Locate every blood parasite and identify its species.
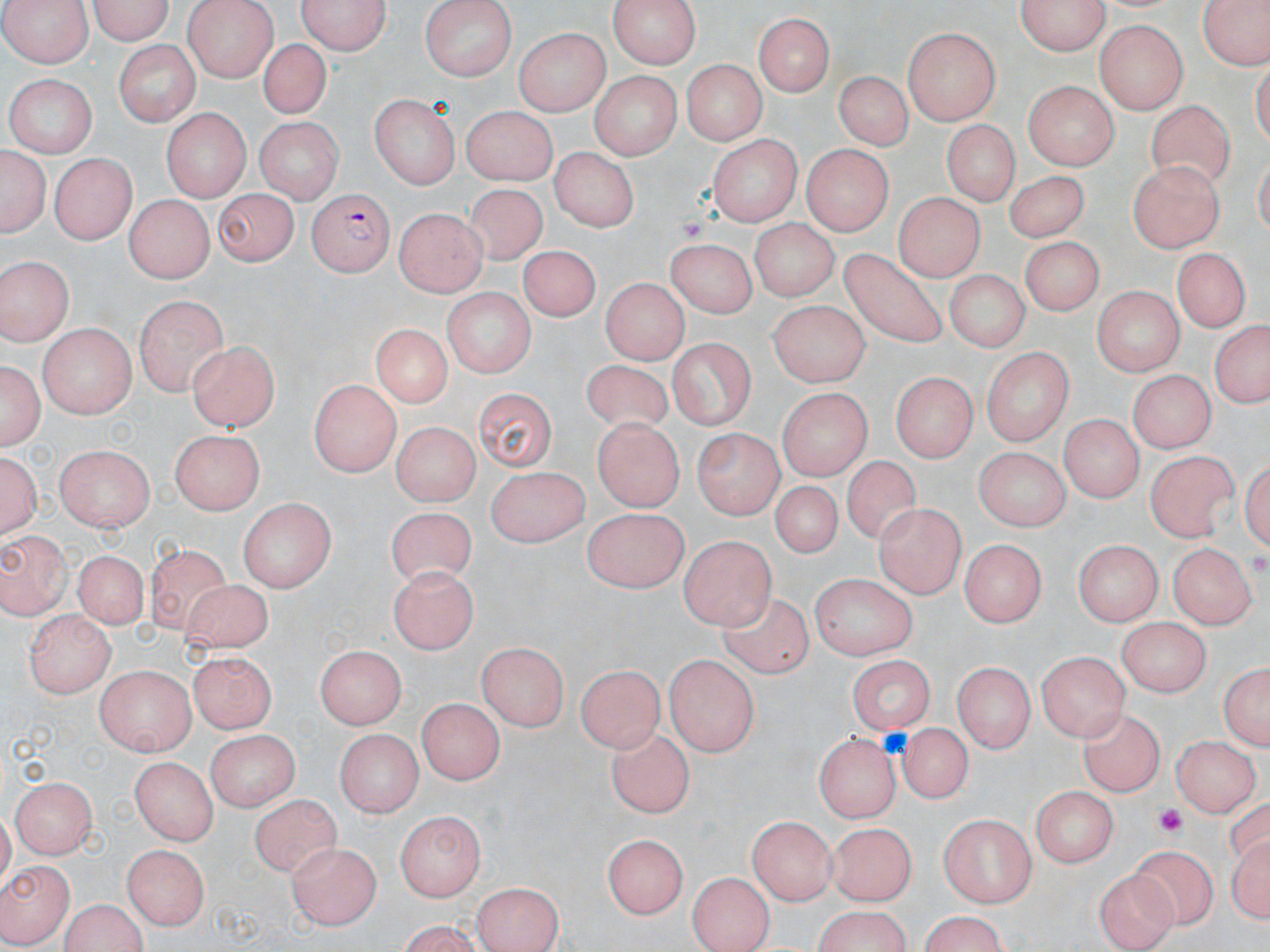

Approximate bounding boxes as named x1/y1/x2/y2 corners in pixels.
Plasmodium falciparum-infected red blood cells: (x1=305, y1=191, x2=393, y2=277).
No Plasmodium ovale, Plasmodium malariae, Plasmodium vivax, Babesia divergens, or Trypanosoma brucei observed.

slide-level diagnosis = Plasmodium falciparum
platelet locations = approximate bounding boxes as named x1/y1/x2/y2 corners in pixels: (x1=678, y1=215, x2=711, y2=245), (x1=1153, y1=802, x2=1192, y2=838)
modality = light microscopy
magnification = 1000x
uninfected red blood cell locations = approximate bounding boxes as named x1/y1/x2/y2 corners in pixels: (x1=83, y1=0, x2=179, y2=43), (x1=182, y1=0, x2=275, y2=79), (x1=296, y1=0, x2=392, y2=56), (x1=419, y1=0, x2=517, y2=78), (x1=606, y1=0, x2=705, y2=69), (x1=1016, y1=0, x2=1111, y2=55), (x1=1199, y1=0, x2=1267, y2=74), (x1=2, y1=1, x2=93, y2=68), (x1=1034, y1=9, x2=1162, y2=81), (x1=754, y1=10, x2=837, y2=97), (x1=1096, y1=20, x2=1188, y2=112), (x1=515, y1=26, x2=607, y2=112), (x1=904, y1=27, x2=1004, y2=124), (x1=256, y1=38, x2=334, y2=118), (x1=113, y1=40, x2=200, y2=126), (x1=679, y1=58, x2=765, y2=145), (x1=586, y1=70, x2=681, y2=160), (x1=836, y1=70, x2=908, y2=151), (x1=4, y1=74, x2=98, y2=155), (x1=1021, y1=79, x2=1120, y2=167), (x1=367, y1=95, x2=461, y2=189), (x1=1147, y1=97, x2=1235, y2=196), (x1=458, y1=105, x2=558, y2=183), (x1=163, y1=111, x2=248, y2=201), (x1=255, y1=119, x2=340, y2=202), (x1=943, y1=121, x2=1023, y2=208), (x1=706, y1=131, x2=802, y2=224), (x1=800, y1=144, x2=896, y2=233), (x1=2, y1=146, x2=49, y2=237), (x1=548, y1=148, x2=639, y2=231), (x1=48, y1=154, x2=137, y2=245), (x1=1127, y1=161, x2=1224, y2=254), (x1=1006, y1=167, x2=1088, y2=242), (x1=460, y1=182, x2=559, y2=270), (x1=210, y1=191, x2=297, y2=266), (x1=895, y1=192, x2=980, y2=281), (x1=121, y1=197, x2=212, y2=285), (x1=395, y1=205, x2=486, y2=295), (x1=747, y1=220, x2=837, y2=306), (x1=1025, y1=235, x2=1104, y2=313), (x1=671, y1=238, x2=755, y2=315), (x1=516, y1=247, x2=606, y2=330), (x1=1173, y1=247, x2=1252, y2=330), (x1=840, y1=248, x2=951, y2=353), (x1=0, y1=255, x2=72, y2=345), (x1=947, y1=267, x2=1029, y2=356), (x1=602, y1=278, x2=686, y2=367), (x1=1094, y1=285, x2=1182, y2=380), (x1=442, y1=287, x2=537, y2=378), (x1=135, y1=294, x2=228, y2=394), (x1=769, y1=298, x2=872, y2=385), (x1=37, y1=321, x2=136, y2=416), (x1=1206, y1=322, x2=1270, y2=411), (x1=365, y1=323, x2=459, y2=407), (x1=669, y1=340, x2=755, y2=428), (x1=187, y1=341, x2=278, y2=433), (x1=980, y1=347, x2=1073, y2=445), (x1=1, y1=356, x2=45, y2=454), (x1=581, y1=359, x2=677, y2=438), (x1=1128, y1=369, x2=1211, y2=452), (x1=893, y1=373, x2=975, y2=463), (x1=307, y1=383, x2=402, y2=474), (x1=474, y1=386, x2=558, y2=470), (x1=781, y1=387, x2=874, y2=477), (x1=1061, y1=413, x2=1141, y2=506), (x1=592, y1=419, x2=683, y2=511), (x1=389, y1=421, x2=480, y2=507), (x1=169, y1=426, x2=267, y2=513), (x1=694, y1=428, x2=782, y2=520), (x1=57, y1=445, x2=154, y2=532), (x1=978, y1=447, x2=1067, y2=534), (x1=1, y1=450, x2=42, y2=542), (x1=1149, y1=451, x2=1242, y2=542), (x1=840, y1=456, x2=927, y2=548), (x1=483, y1=466, x2=590, y2=548), (x1=768, y1=480, x2=845, y2=558), (x1=235, y1=500, x2=337, y2=593), (x1=874, y1=501, x2=964, y2=598), (x1=382, y1=506, x2=475, y2=595), (x1=584, y1=509, x2=686, y2=595), (x1=0, y1=528, x2=74, y2=617), (x1=680, y1=533, x2=773, y2=628), (x1=955, y1=537, x2=1041, y2=622), (x1=1076, y1=539, x2=1162, y2=628), (x1=1170, y1=542, x2=1254, y2=631), (x1=144, y1=544, x2=230, y2=641), (x1=73, y1=552, x2=150, y2=627), (x1=389, y1=566, x2=476, y2=652), (x1=811, y1=575, x2=918, y2=663), (x1=173, y1=578, x2=278, y2=662), (x1=717, y1=592, x2=816, y2=680), (x1=23, y1=612, x2=114, y2=699), (x1=1115, y1=616, x2=1209, y2=695), (x1=477, y1=642, x2=569, y2=733), (x1=314, y1=646, x2=403, y2=732), (x1=1037, y1=648, x2=1130, y2=740), (x1=193, y1=649, x2=275, y2=729), (x1=665, y1=654, x2=759, y2=757), (x1=848, y1=655, x2=933, y2=737), (x1=1218, y1=659, x2=1270, y2=755), (x1=954, y1=660, x2=1033, y2=756), (x1=579, y1=663, x2=662, y2=754), (x1=97, y1=665, x2=198, y2=755), (x1=419, y1=700, x2=501, y2=786), (x1=1080, y1=706, x2=1165, y2=795), (x1=902, y1=720, x2=971, y2=801), (x1=336, y1=728, x2=421, y2=818), (x1=608, y1=729, x2=695, y2=817), (x1=814, y1=731, x2=899, y2=823), (x1=208, y1=733, x2=300, y2=809), (x1=1174, y1=734, x2=1258, y2=818), (x1=132, y1=756, x2=216, y2=845), (x1=14, y1=776, x2=96, y2=856), (x1=1027, y1=784, x2=1120, y2=866), (x1=250, y1=794, x2=343, y2=879), (x1=396, y1=809, x2=488, y2=900), (x1=936, y1=815, x2=1037, y2=906), (x1=750, y1=817, x2=838, y2=903), (x1=832, y1=826, x2=915, y2=904), (x1=602, y1=834, x2=685, y2=920), (x1=1227, y1=837, x2=1268, y2=923), (x1=292, y1=842, x2=380, y2=925), (x1=123, y1=843, x2=211, y2=931), (x1=1124, y1=848, x2=1217, y2=932), (x1=0, y1=860, x2=76, y2=942), (x1=1093, y1=866, x2=1177, y2=951), (x1=689, y1=870, x2=777, y2=951), (x1=472, y1=879, x2=563, y2=952), (x1=55, y1=897, x2=151, y2=952), (x1=810, y1=908, x2=916, y2=952), (x1=913, y1=915, x2=1014, y2=950), (x1=383, y1=921, x2=489, y2=950)
field of view = single
image size = 1270×952 pixels
stain = May-Grünwald-Giemsa
preparation = thin blood smear